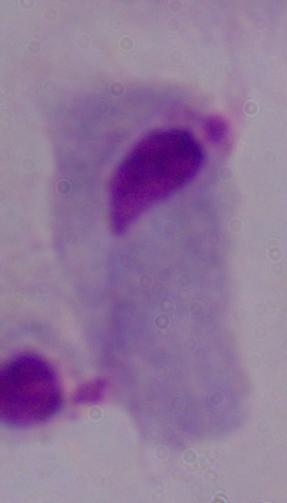 Photomicrograph. A trichomonad is shown. Captured at 1000x magnification.